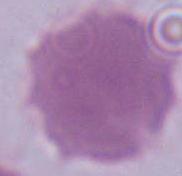

Photomicrograph. Captured at 1000x magnification. A red blood cell is shown.